Assess this cell for malaria.
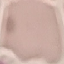
It is uninfected.

capture: smartphone through the microscope eyepiece
image_type: cell patch, automatically extracted from a larger field of view and resized to 64 × 64 pixels
stain: Giemsa
preparation: thin smear